Name the blood parasite species.
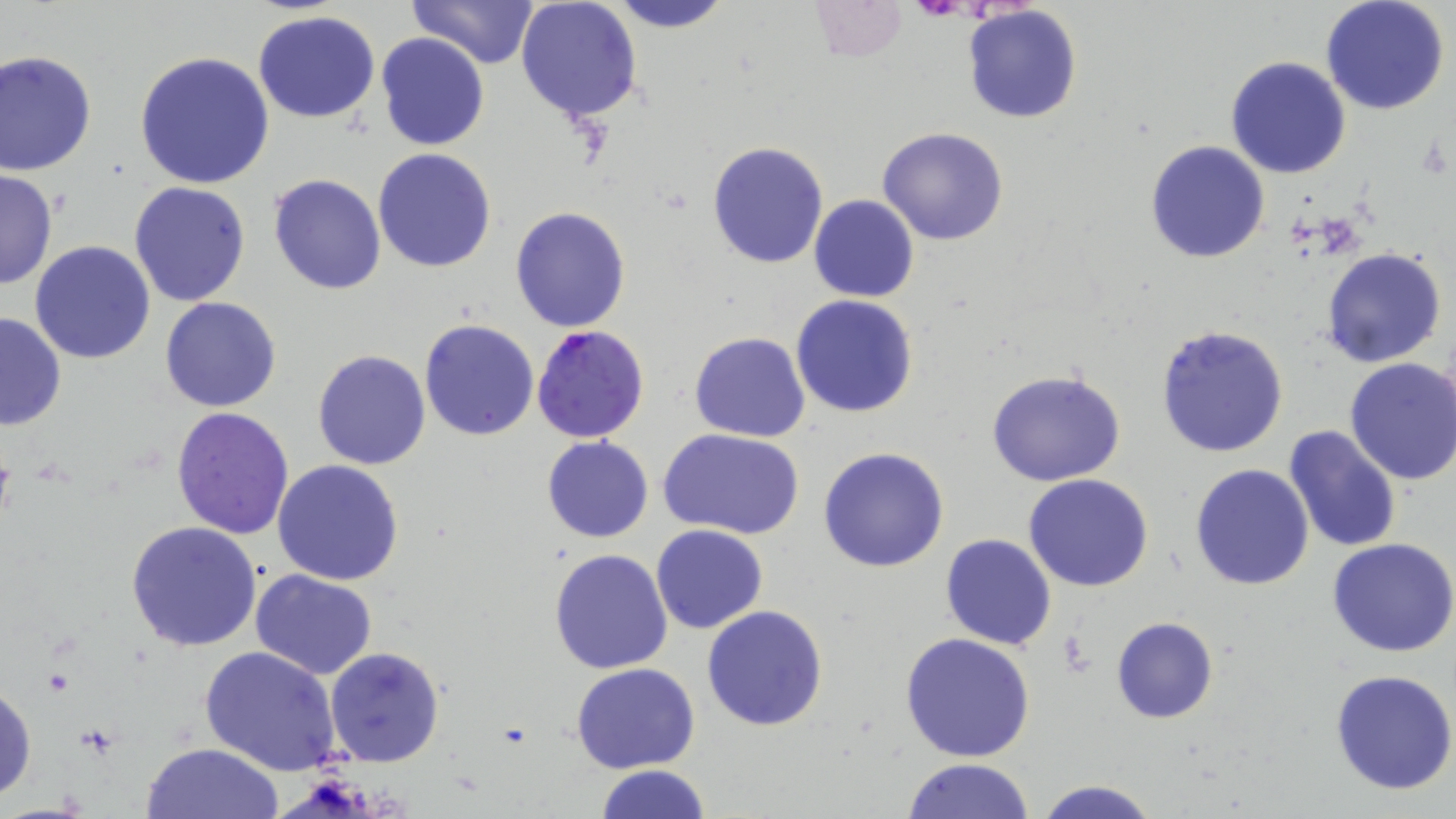
Plasmodium falciparum.

Summary:
  - Coordinate format: approximate bounding boxes as (x1, y1, x2, y2) in pixels
  - Platelet locations: (1059, 630, 1095, 674)
  - Plasmodium falciparum-infected red blood cell locations: (531, 325, 650, 444)
  - Uninfected red blood cell locations: (407, 0, 538, 70), (604, 0, 734, 32), (806, 0, 907, 63), (515, 1, 642, 123), (1321, 1, 1450, 116), (961, 5, 1082, 124), (253, 11, 381, 124), (375, 33, 489, 151), (0, 51, 97, 176), (134, 52, 275, 189), (1225, 56, 1351, 179), (876, 127, 1009, 246), (1144, 139, 1270, 264), (706, 140, 830, 268), (371, 148, 497, 272), (0, 170, 58, 292), (268, 173, 386, 294), (129, 182, 251, 306), (809, 194, 921, 304), (510, 206, 630, 332), (30, 240, 155, 364), (1321, 247, 1448, 368), (790, 294, 919, 418), (159, 296, 282, 412), (0, 310, 67, 430), (418, 318, 540, 441), (1156, 324, 1289, 458), (689, 332, 810, 442), (312, 348, 431, 469), (1343, 358, 1456, 486), (985, 368, 1126, 486), (170, 406, 294, 540), (1282, 425, 1400, 552), (659, 426, 805, 539), (541, 435, 654, 542), (818, 447, 949, 572), (272, 460, 405, 587), (1189, 462, 1314, 591), (1022, 475, 1153, 592), (126, 522, 262, 651), (651, 525, 769, 634), (940, 533, 1057, 649), (1328, 538, 1456, 658), (548, 548, 674, 674), (250, 569, 376, 679), (701, 605, 830, 732), (1110, 615, 1217, 723), (899, 632, 1036, 762), (198, 644, 341, 776), (325, 645, 447, 768), (571, 662, 699, 774), (1330, 669, 1456, 794), (0, 679, 36, 804), (141, 742, 286, 819), (902, 758, 1036, 818), (596, 765, 710, 819), (1031, 778, 1164, 819)
  - Modality: light microscopy
  - Image size: 1456×819 pixels
  - Field of view: single
  - Magnification: 1000x
  - Stain: May-Grünwald-Giemsa
  - Preparation: thin blood smear